Comment on the morphology of the red blood cells.
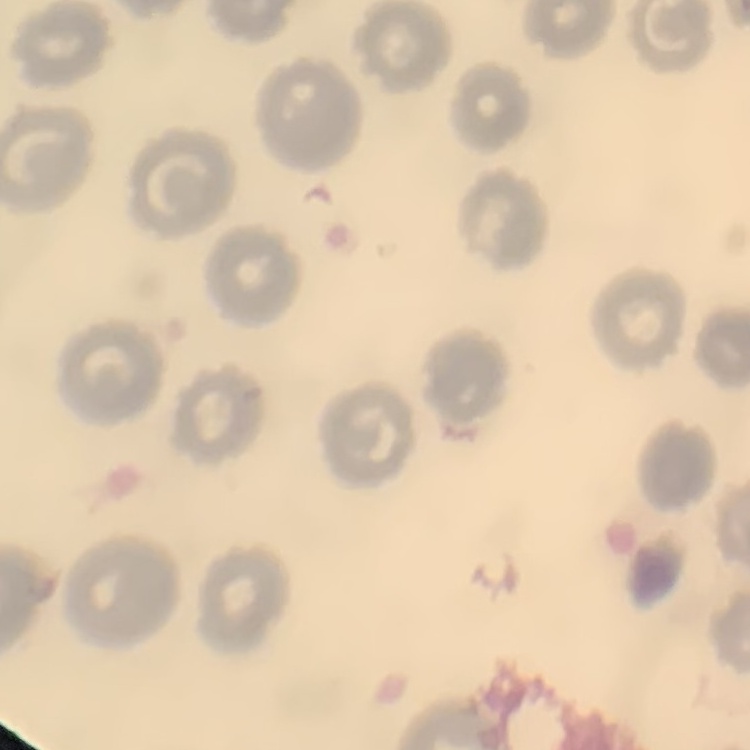

No rouleaux formation.

preparation = thin peripheral smear
stain = Field's or Giemsa
image type = square crop of a larger photomicrograph